Give the position of every malaria parasite.
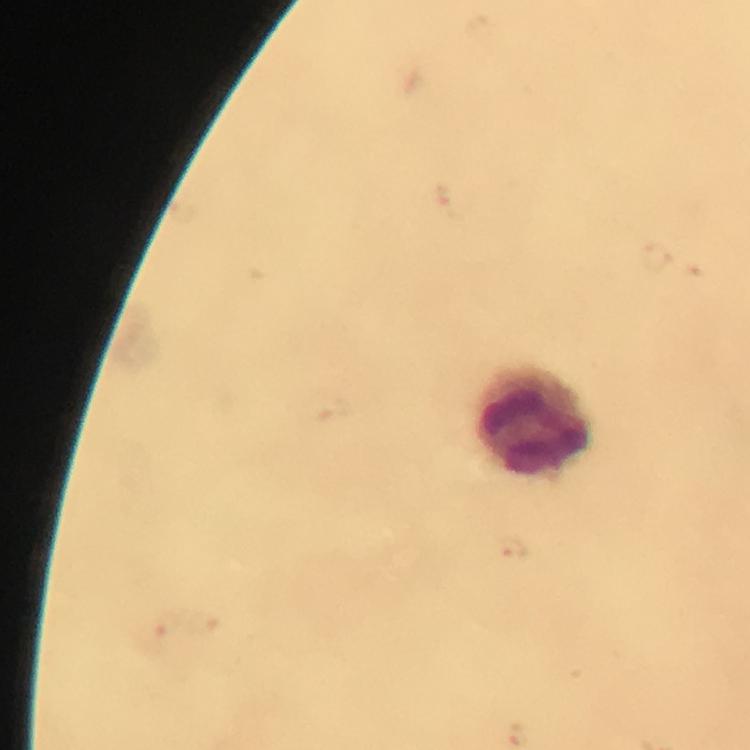

Approximate centers as (x, y) in pixels.
Malaria parasites: (513, 548).

leukocyte_locations: 'approximate centers as (x, y) in pixels: (533, 423)'
magnification: 100x
capture: smartphone camera through the microscope
image_size: 750×750 pixels
cropped_from: one field of view
preparation: thick smear
context: from a diagnostic examination for malaria
stain: Giemsa
immersion_oil: used